Point out every Plasmodium parasite.
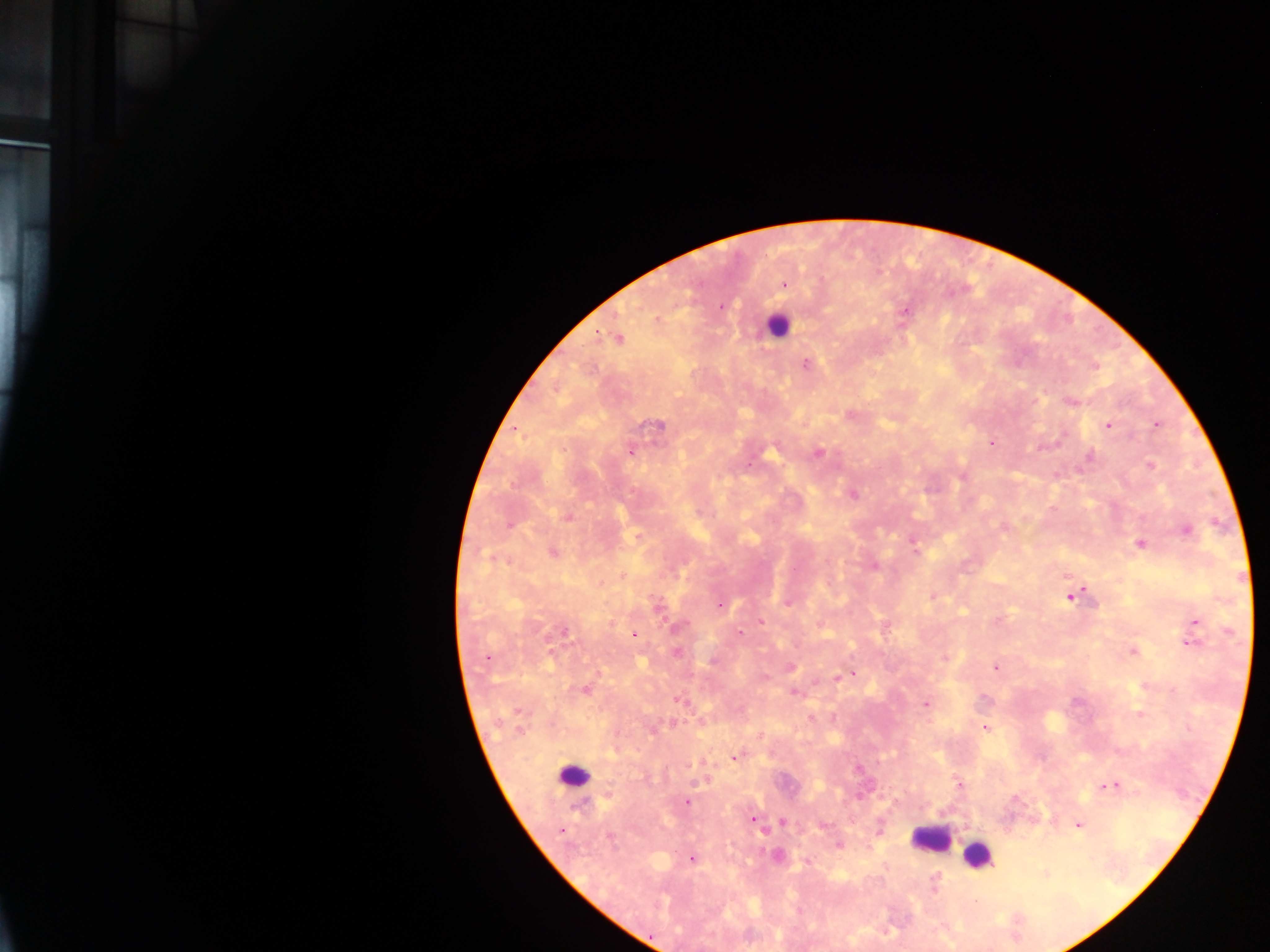

Approximate centers as (x, y) in pixels.
Plasmodium parasites: (783, 284), (719, 306), (903, 311), (656, 320), (618, 337), (806, 364), (1094, 366), (1070, 402), (850, 414), (1156, 424), (658, 425), (1107, 425), (992, 443), (631, 450), (817, 454), (1089, 456), (1150, 466), (852, 494), (567, 516), (1003, 527), (1186, 528), (912, 543), (1139, 544), (553, 552), (874, 565), (1079, 593), (1069, 596), (931, 597), (788, 602), (720, 604), (656, 606), (1193, 621), (760, 622), (563, 631), (740, 632), (633, 635), (1189, 643), (1133, 651), (677, 652), (487, 656), (945, 659), (790, 666), (995, 667), (854, 673), (846, 676), (837, 677), (585, 689), (794, 691), (679, 700), (926, 703), (1139, 714), (985, 727), (734, 757), (703, 763), (706, 779), (959, 784), (1110, 786), (686, 801), (751, 819), (781, 821), (1078, 825), (561, 830), (838, 845), (777, 855), (691, 858), (805, 861), (934, 879).

field of view = single
leukocyte locations = approximate centers as (x, y) in pixels: (777, 325), (572, 776), (931, 838), (978, 855)
capture = mobile-phone photograph through a microscope
preparation = thick blood film
country = Ghana
image size = 1270×952 pixels